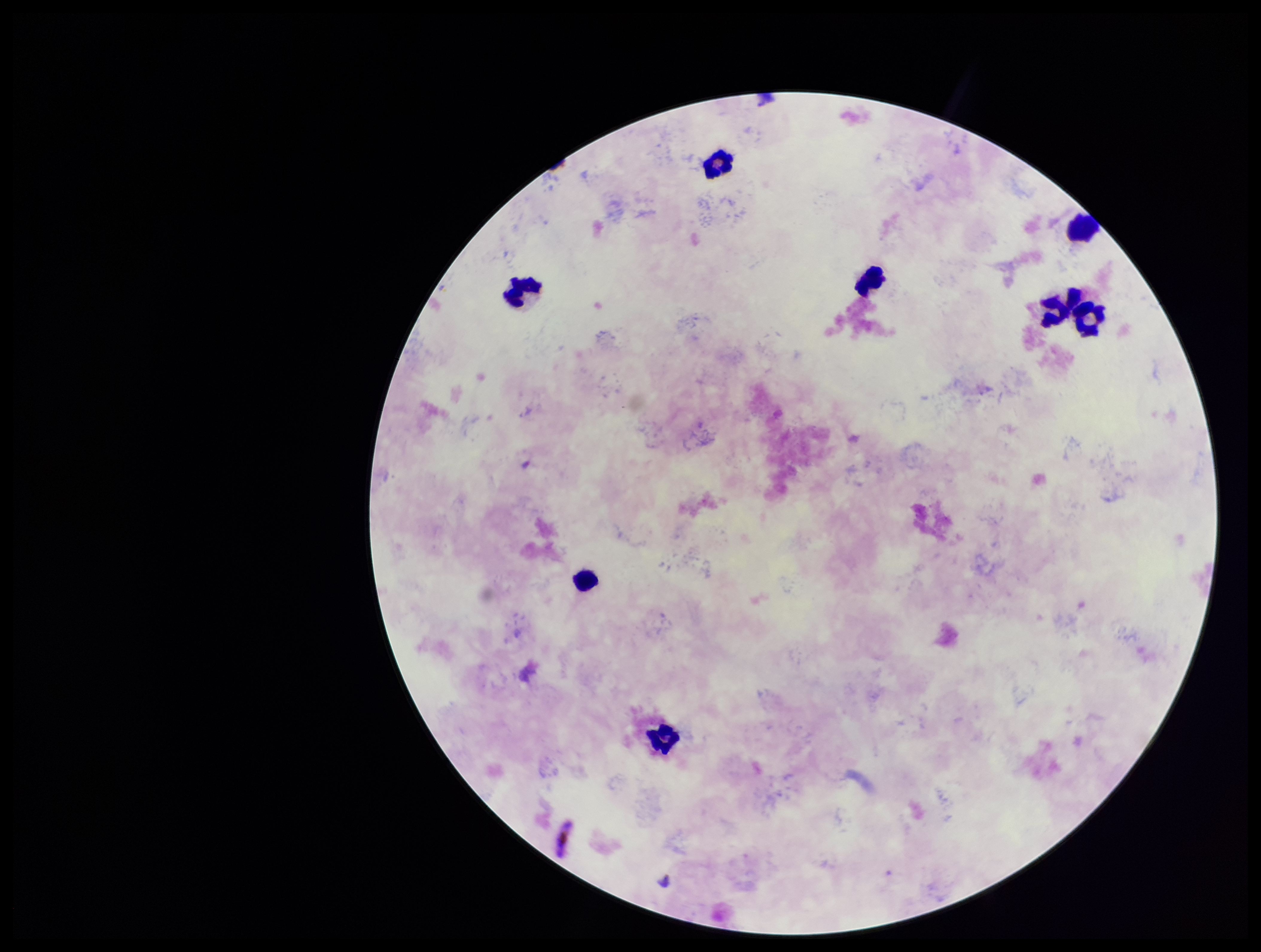
Summary:
  - Field of view: single
  - Parasite count: 0
  - Preparation: thick smear
  - Leukocyte count: 8
  - Image size: 1261×952 pixels
  - Capture: smartphone photograph through the microscope eyepiece
  - Stain: Giemsa
  - Species reported for this patient: Plasmodium falciparum
  - Patient malaria status: infected
  - Plasmodium parasites: none detected